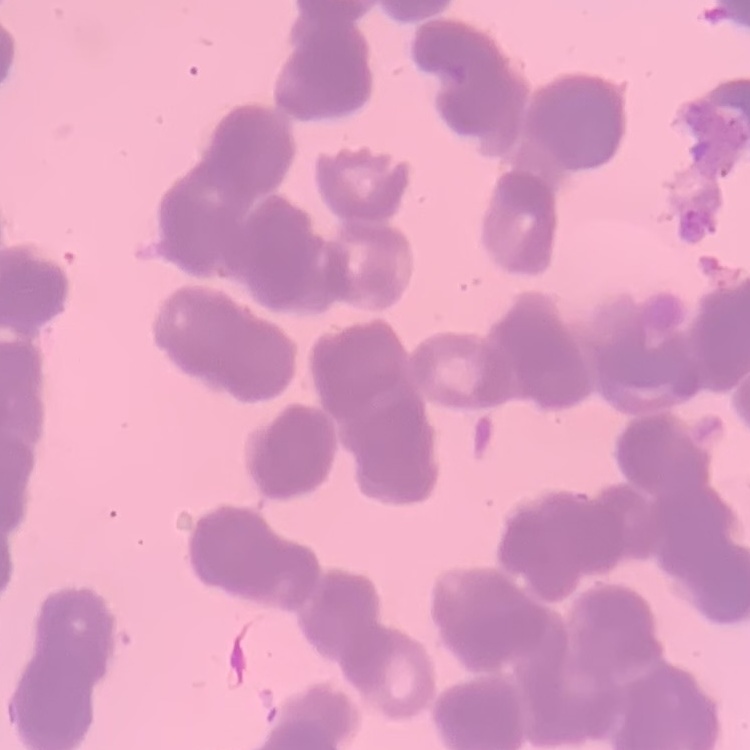

The red blood cells show rouleaux formation. Square crop of a larger photomicrograph. Thin peripheral smear. Field's or Giemsa stain.